Assess this cell for malaria.
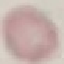

It is uninfected.

{
  "stain": "Giemsa",
  "preparation": "thin blood smear",
  "image_type": "automatically extracted cell patch, resized to 64 × 64 pixels",
  "capture": "smartphone through the microscope eyepiece"
}